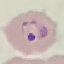 Result: malaria parasites detected. Cell patch, automatically extracted from a larger field of view and resized to 64 × 64 pixels. Thin smear of blood. Acquired by smartphone through the microscope eyepiece. Giemsa stain.